Comment on the morphology of the red blood cells.
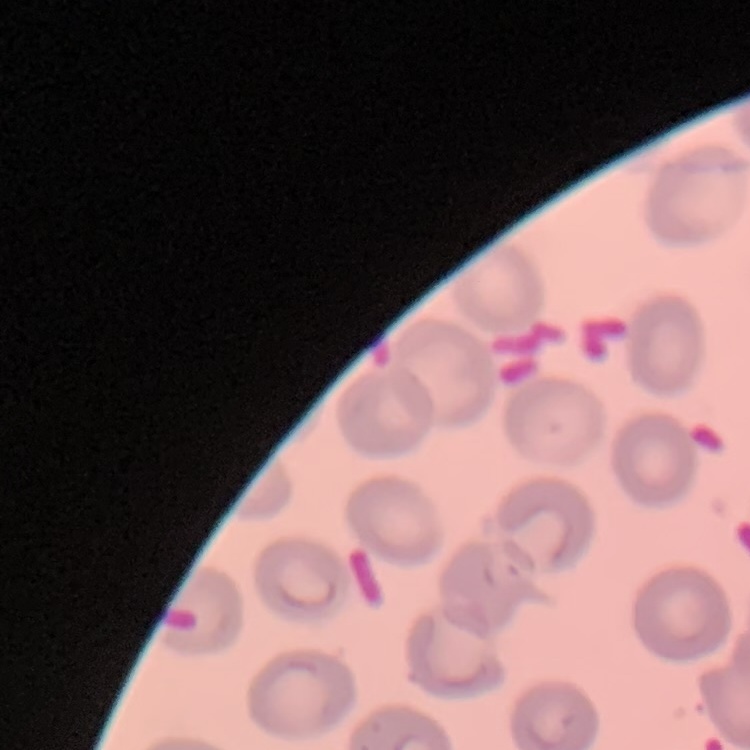
They show no rouleaux formation.

preparation = thin blood film
image type = one tile cut from a larger photomicrograph
stain = Field's or Giemsa